Locate every Plasmodium parasite.
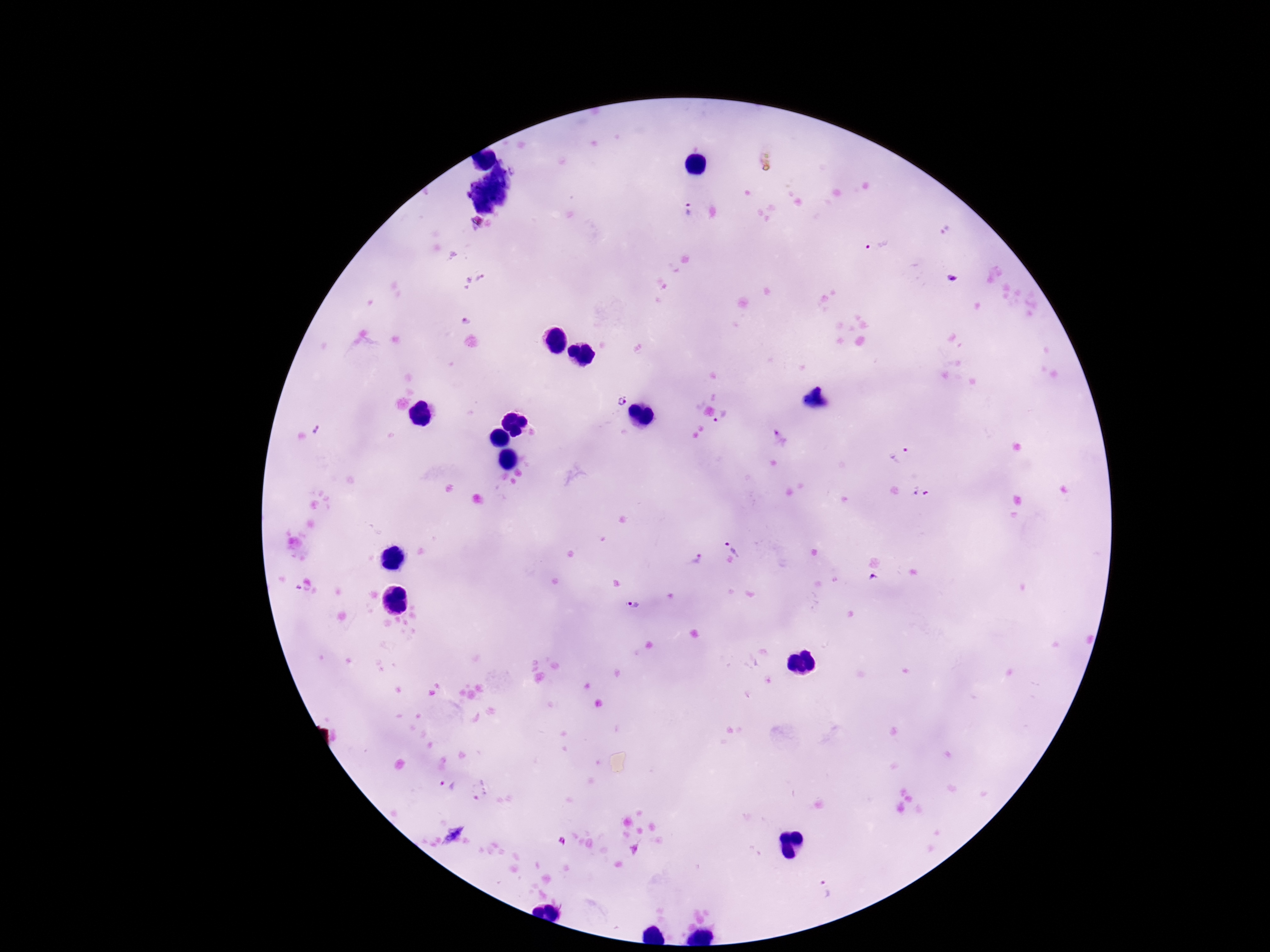
Approximate centers as {x, y} in pixels.
Plasmodium parasites: {687, 209}, {878, 246}, {480, 280}, {619, 401}, {723, 417}, {317, 428}, {780, 438}, {900, 460}, {922, 492}, {735, 545}, {695, 557}, {874, 580}, {632, 604}, {448, 786}, {479, 792}, {823, 889}.

Summary:
  - Image size: 1270×952 pixels
  - Stain: Giemsa
  - Preparation: thick peripheral-blood smear
  - Magnification: 100x
  - Capture: smartphone camera through the microscope eyepiece
  - Field of view: one from this slide
  - Patient malaria status: infected